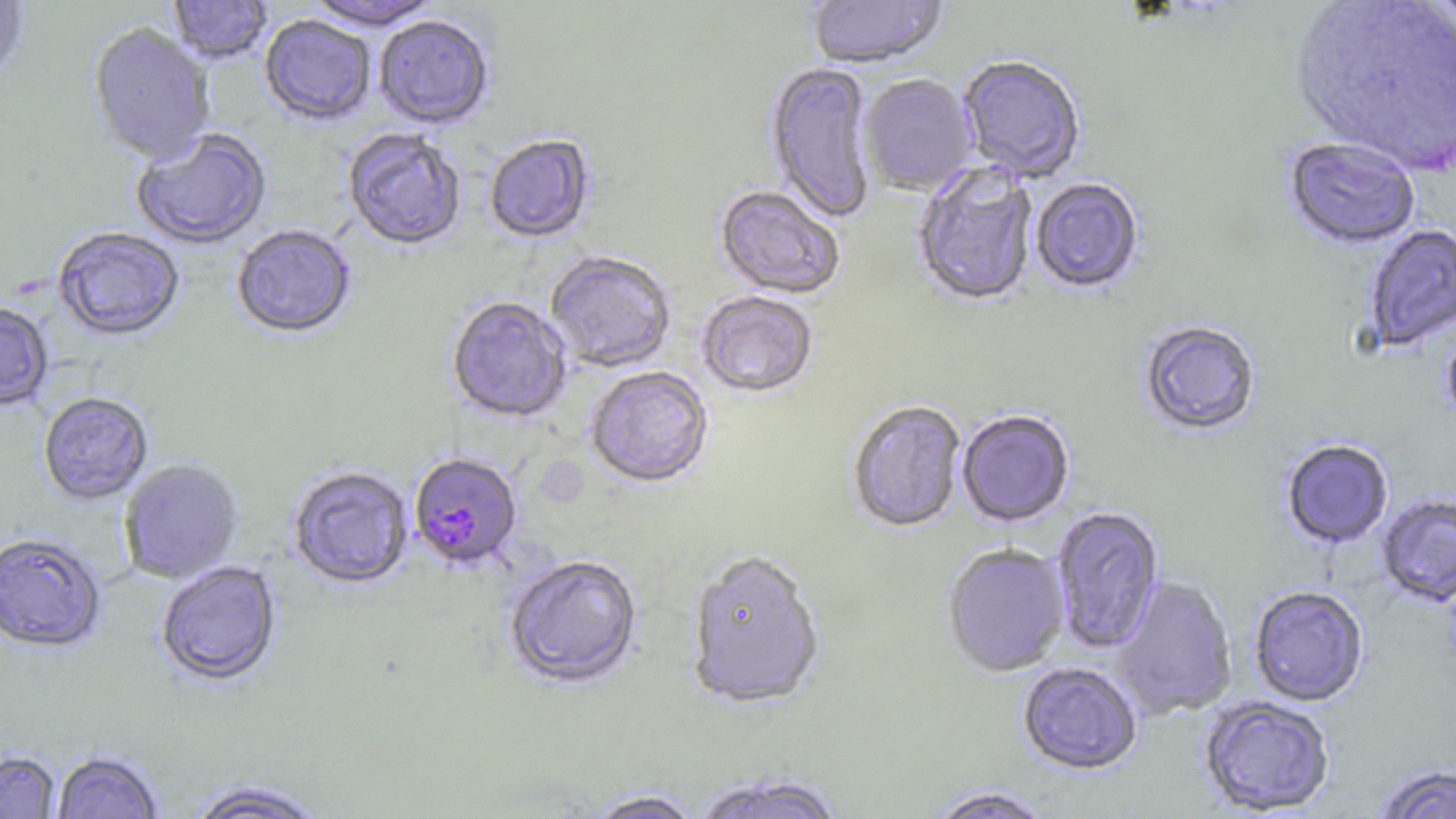
Summary:
  - Coordinate format: approximate bounding boxes as (x1, y1, x2, y2) in pixels
  - Plasmodium falciparum-infected red blood cell locations: (409, 454, 523, 572)
  - Uninfected red blood cell locations: (0, 0, 30, 83), (169, 0, 273, 66), (304, 0, 443, 33), (807, 0, 947, 71), (1424, 0, 1456, 37), (1289, 1, 1456, 179), (260, 17, 376, 128), (374, 18, 494, 131), (88, 23, 215, 166), (956, 56, 1086, 185), (765, 62, 877, 224), (860, 75, 979, 196), (132, 129, 272, 250), (343, 130, 466, 252), (484, 136, 596, 244), (1283, 139, 1420, 251), (912, 165, 1039, 309), (1030, 179, 1145, 295), (715, 186, 845, 300), (1363, 224, 1456, 353), (232, 225, 356, 341), (53, 228, 185, 343), (545, 252, 675, 373), (697, 292, 818, 399), (446, 298, 571, 425), (0, 303, 53, 413), (1441, 320, 1456, 431), (1139, 322, 1260, 437), (585, 367, 714, 491), (38, 393, 153, 506), (847, 402, 966, 534), (957, 411, 1075, 528), (1281, 439, 1394, 549), (119, 459, 244, 584), (288, 467, 414, 591), (1377, 494, 1456, 608), (1050, 506, 1165, 655), (0, 534, 106, 655), (942, 544, 1070, 678), (685, 553, 826, 714), (504, 556, 642, 691), (156, 562, 281, 688), (1111, 576, 1238, 719), (1249, 587, 1369, 707), (1017, 662, 1143, 776), (1199, 695, 1336, 816), (0, 751, 61, 818), (51, 751, 164, 818), (1372, 764, 1456, 819), (689, 772, 850, 819), (185, 780, 330, 818), (924, 787, 1055, 818), (586, 789, 704, 818)
  - Slide-level diagnosis: Plasmodium falciparum
  - Modality: optical microscopy
  - Image size: 1456×819 pixels
  - Stain: May-Grünwald-Giemsa
  - Preparation: thin blood smear
  - Field of view: one of a larger specimen
  - Magnification: 1000x